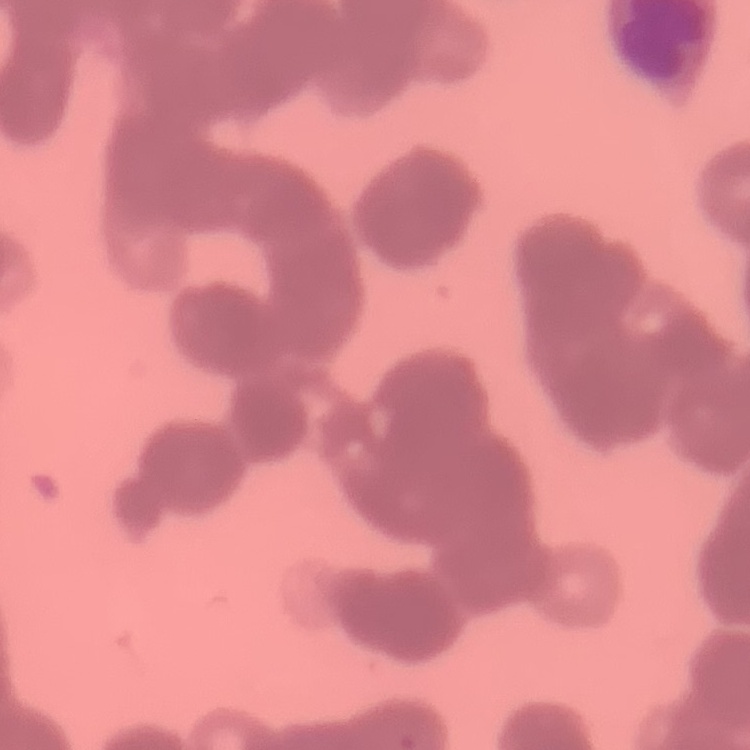 The erythrocytes exhibit rouleaux formation. Thin blood film. Field's or Giemsa stain. Square crop of a larger photomicrograph.